Identify the blood parasite species.
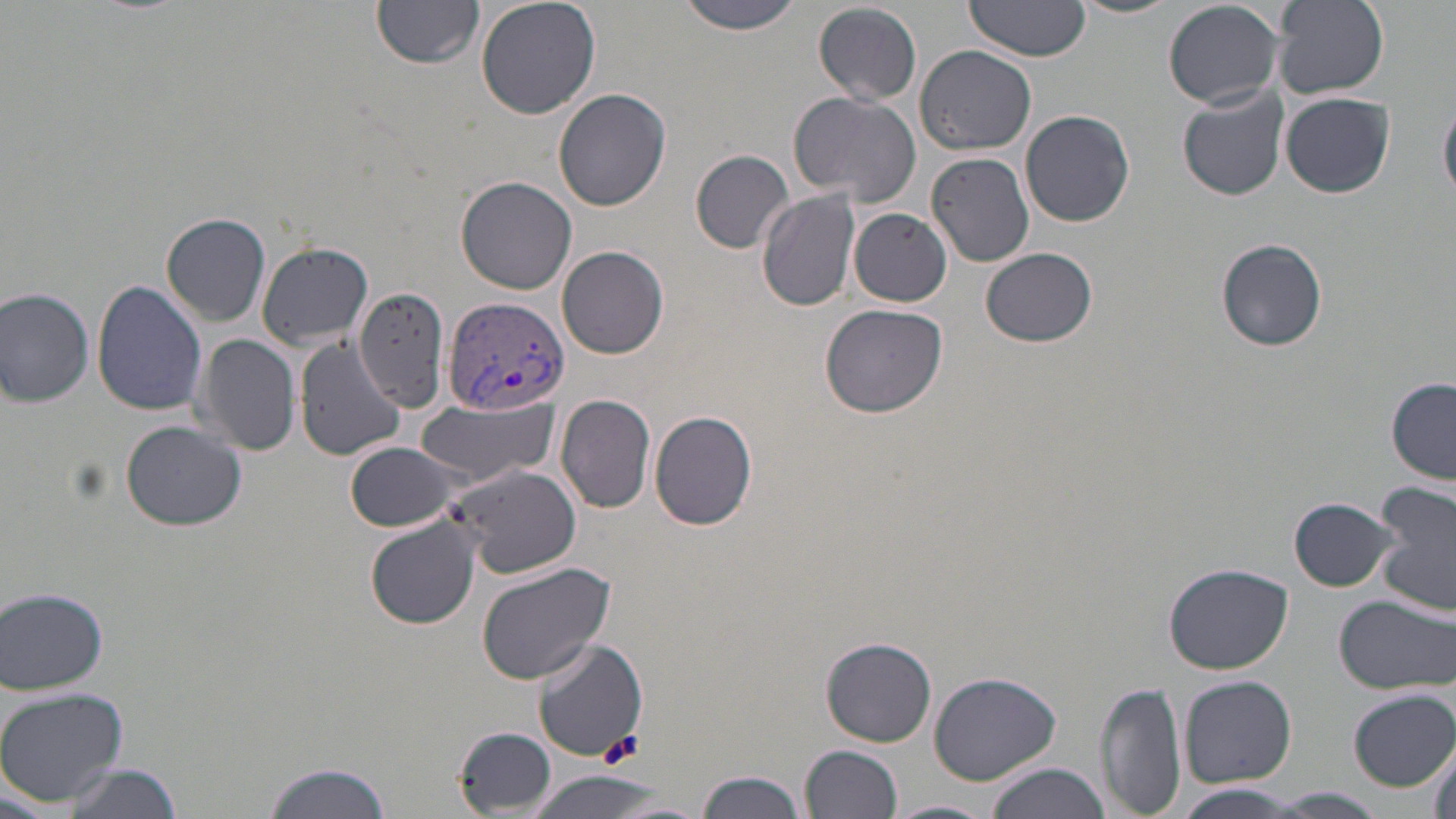

Plasmodium vivax.

image_size: 1456×819 pixels
preparation: thin blood smear
plasmodium_vivax_infected_red_blood_cell_locations: 'approximate bounding boxes as [x1, y1, x2, y2] in pixels: [442, 296, 570, 418]'
stain: May-Grünwald-Giemsa
platelet_locations: 'approximate bounding boxes as [x1, y1, x2, y2] in pixels: [600, 730, 644, 764]'
modality: optical microscopy
magnification: 1000x
uninfected_red_blood_cell_locations: 'approximate bounding boxes as [x1, y1, x2, y2] in pixels: [372, 0, 485, 70], [476, 0, 601, 120], [677, 0, 806, 36], [1068, 0, 1182, 19], [1163, 0, 1287, 108], [1273, 0, 1389, 98], [963, 1, 1095, 66], [814, 3, 922, 106], [916, 45, 1038, 156], [1177, 87, 1288, 201], [553, 89, 672, 212], [1280, 91, 1395, 197], [788, 92, 922, 205], [1440, 92, 1456, 203], [1022, 109, 1135, 226], [691, 148, 793, 252], [926, 152, 1035, 268], [455, 176, 578, 295], [757, 191, 863, 311], [850, 209, 951, 306], [161, 213, 272, 326], [1216, 237, 1326, 350], [256, 242, 374, 351], [558, 245, 669, 358], [981, 248, 1097, 348], [91, 279, 208, 416], [352, 284, 451, 411], [0, 287, 96, 408], [820, 303, 950, 418], [196, 334, 301, 458], [294, 338, 408, 460], [1387, 379, 1455, 485], [557, 394, 657, 513], [415, 399, 558, 487], [649, 410, 760, 529], [120, 419, 246, 531], [344, 442, 464, 532], [442, 464, 582, 579], [1372, 482, 1456, 618], [1290, 496, 1401, 591], [367, 516, 482, 631], [474, 560, 617, 684], [1165, 563, 1293, 674], [1, 586, 110, 696], [1334, 593, 1456, 696], [820, 636, 937, 747], [531, 638, 648, 763], [929, 670, 1061, 784], [1179, 675, 1296, 787], [1095, 681, 1186, 818], [0, 687, 129, 807], [1349, 688, 1455, 793], [453, 727, 556, 814], [1428, 732, 1454, 819], [800, 745, 904, 818], [261, 760, 394, 819], [58, 762, 182, 819], [983, 763, 1109, 819], [522, 770, 677, 819], [696, 770, 807, 819], [1167, 788, 1320, 818], [1264, 789, 1386, 817], [880, 800, 997, 819]'
field_of_view: one of a larger specimen